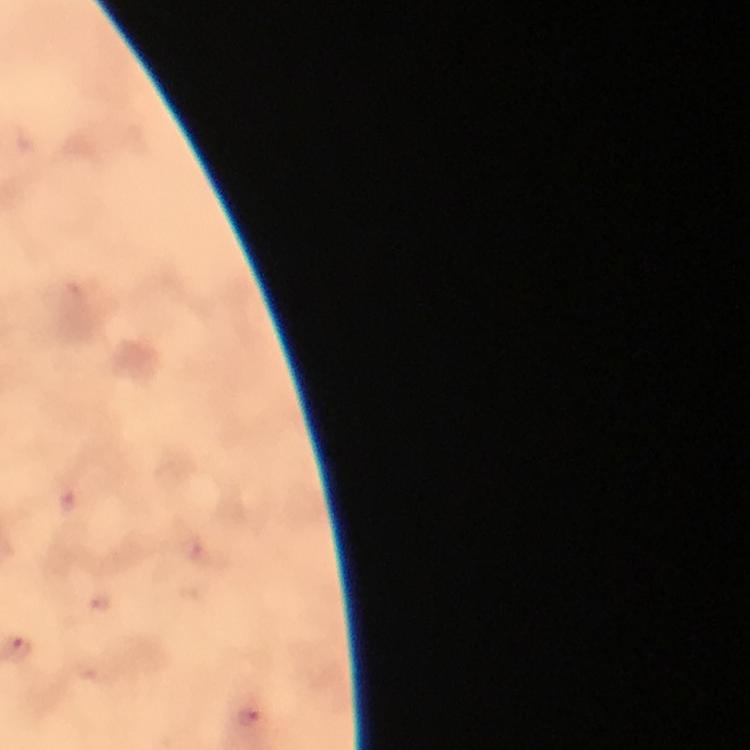
Approximate centers as [x, y] in pixels. Plasmodium parasite locations: [17, 650], [249, 717]. Thick blood smear. Photographed with a smartphone mounted on the microscope. 100x magnification. Immersion oil applied. Cropped region of a single field of view. From a malaria diagnostic workup. Image is 750×750 pixels. Giemsa stain.